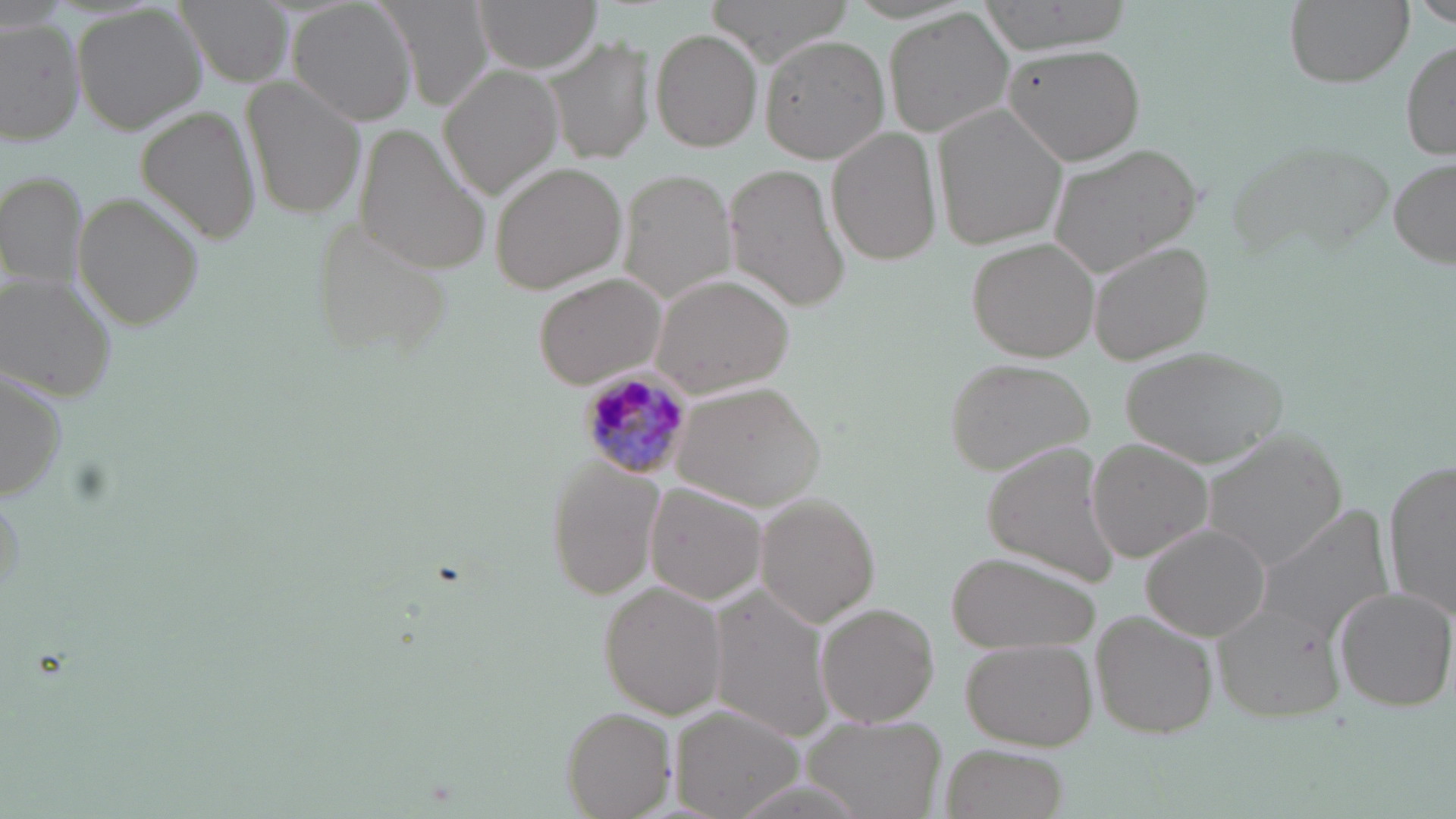
Approximate bounding boxes as named x1/y1/x2/y2 corners in pixels. Plasmodium malariae-infected red blood cell locations: (x1=580, y1=369, x2=694, y2=479). Uninfected red blood cell locations: (x1=175, y1=0, x2=291, y2=83), (x1=291, y1=0, x2=420, y2=125), (x1=378, y1=0, x2=495, y2=111), (x1=475, y1=0, x2=601, y2=71), (x1=705, y1=0, x2=854, y2=67), (x1=969, y1=0, x2=1138, y2=55), (x1=1282, y1=0, x2=1412, y2=88), (x1=1417, y1=0, x2=1456, y2=29), (x1=75, y1=4, x2=208, y2=135), (x1=883, y1=7, x2=1018, y2=138), (x1=0, y1=16, x2=86, y2=145), (x1=652, y1=28, x2=763, y2=152), (x1=760, y1=35, x2=887, y2=162), (x1=546, y1=37, x2=654, y2=163), (x1=1401, y1=40, x2=1455, y2=160), (x1=1005, y1=43, x2=1146, y2=167), (x1=439, y1=63, x2=565, y2=202), (x1=244, y1=77, x2=364, y2=220), (x1=136, y1=104, x2=261, y2=244), (x1=932, y1=105, x2=1068, y2=254), (x1=828, y1=127, x2=942, y2=266), (x1=359, y1=130, x2=492, y2=273), (x1=1226, y1=135, x2=1398, y2=261), (x1=1044, y1=142, x2=1203, y2=280), (x1=1388, y1=159, x2=1454, y2=269), (x1=490, y1=162, x2=627, y2=296), (x1=724, y1=165, x2=849, y2=311), (x1=0, y1=170, x2=86, y2=293), (x1=619, y1=170, x2=738, y2=304), (x1=75, y1=194, x2=202, y2=330), (x1=303, y1=209, x2=457, y2=355), (x1=967, y1=237, x2=1100, y2=361), (x1=1091, y1=243, x2=1214, y2=365), (x1=532, y1=272, x2=668, y2=387), (x1=648, y1=274, x2=795, y2=400), (x1=1, y1=275, x2=117, y2=400), (x1=1120, y1=342, x2=1290, y2=469), (x1=947, y1=358, x2=1099, y2=477), (x1=0, y1=368, x2=67, y2=505), (x1=673, y1=381, x2=826, y2=513), (x1=1197, y1=432, x2=1346, y2=574), (x1=1088, y1=438, x2=1216, y2=563), (x1=982, y1=444, x2=1123, y2=581), (x1=1386, y1=454, x2=1456, y2=625), (x1=544, y1=460, x2=667, y2=599), (x1=645, y1=482, x2=767, y2=605), (x1=753, y1=495, x2=879, y2=627), (x1=1257, y1=506, x2=1396, y2=643), (x1=1142, y1=525, x2=1271, y2=641), (x1=952, y1=552, x2=1100, y2=654), (x1=603, y1=581, x2=729, y2=718), (x1=708, y1=586, x2=838, y2=742), (x1=1329, y1=586, x2=1456, y2=714), (x1=816, y1=603, x2=942, y2=729), (x1=1215, y1=604, x2=1348, y2=721), (x1=1091, y1=613, x2=1216, y2=739), (x1=961, y1=637, x2=1096, y2=749), (x1=672, y1=706, x2=804, y2=819), (x1=563, y1=708, x2=677, y2=819), (x1=802, y1=714, x2=947, y2=819), (x1=940, y1=742, x2=1068, y2=819). Slide-level diagnosis: Plasmodium malariae. Captured at 1000x magnification. Light microscopy. Thin blood smear. Image is 1456×819 pixels. May-Grünwald-Giemsa-stained preparation. One field of a larger specimen.